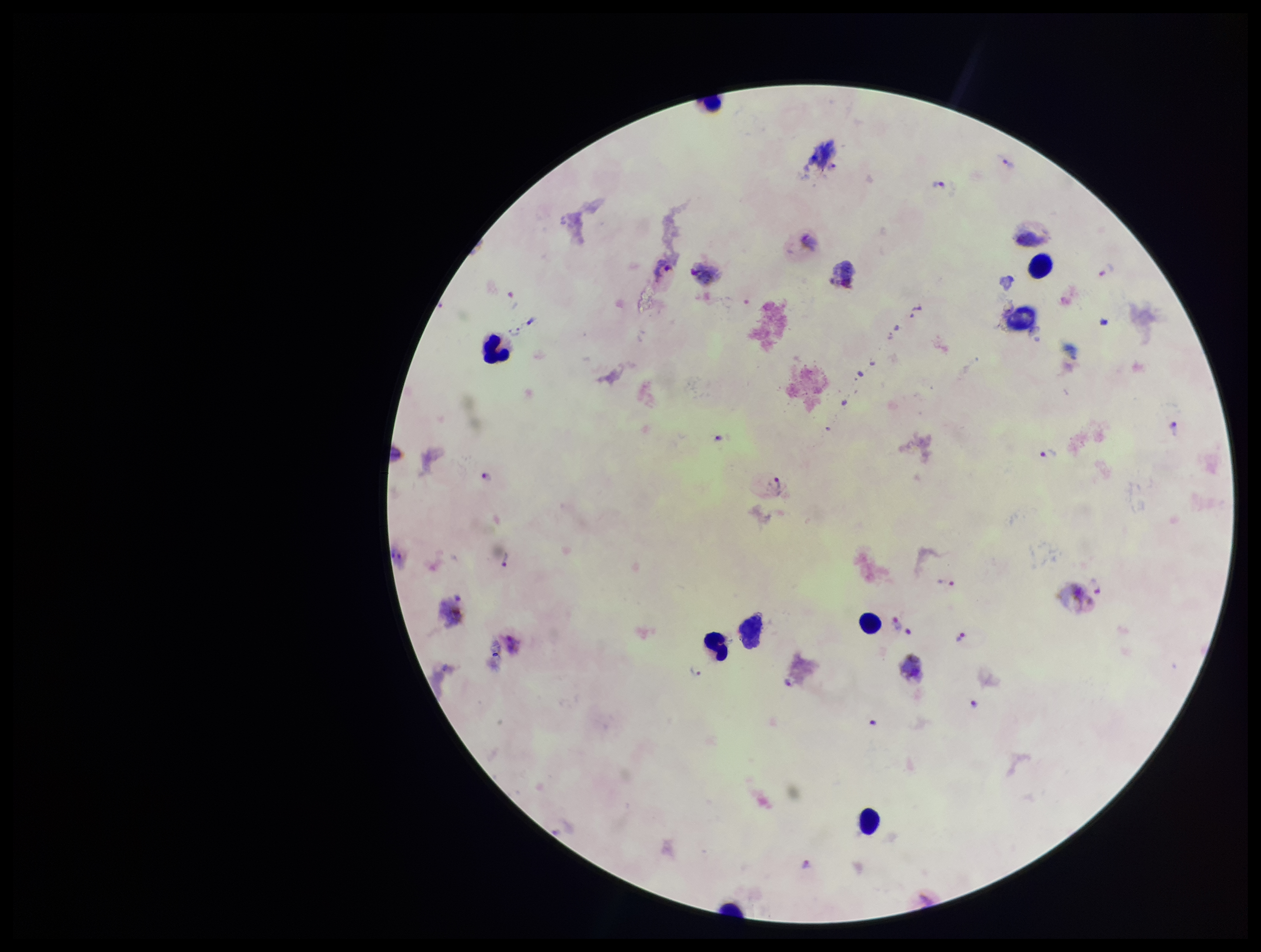

patient malaria status = positive
image size = 1261×952 pixels
field of view = one from this slide
stain = Giemsa
species reported for this patient = Plasmodium vivax
preparation = thick smear
capture = smartphone photograph through the microscope eyepiece
Plasmodium parasites = detected
parasite count = 16
leukocyte count = 5